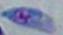
Photomicrograph. Toxoplasma gondii is shown. Captured at 1000x magnification.